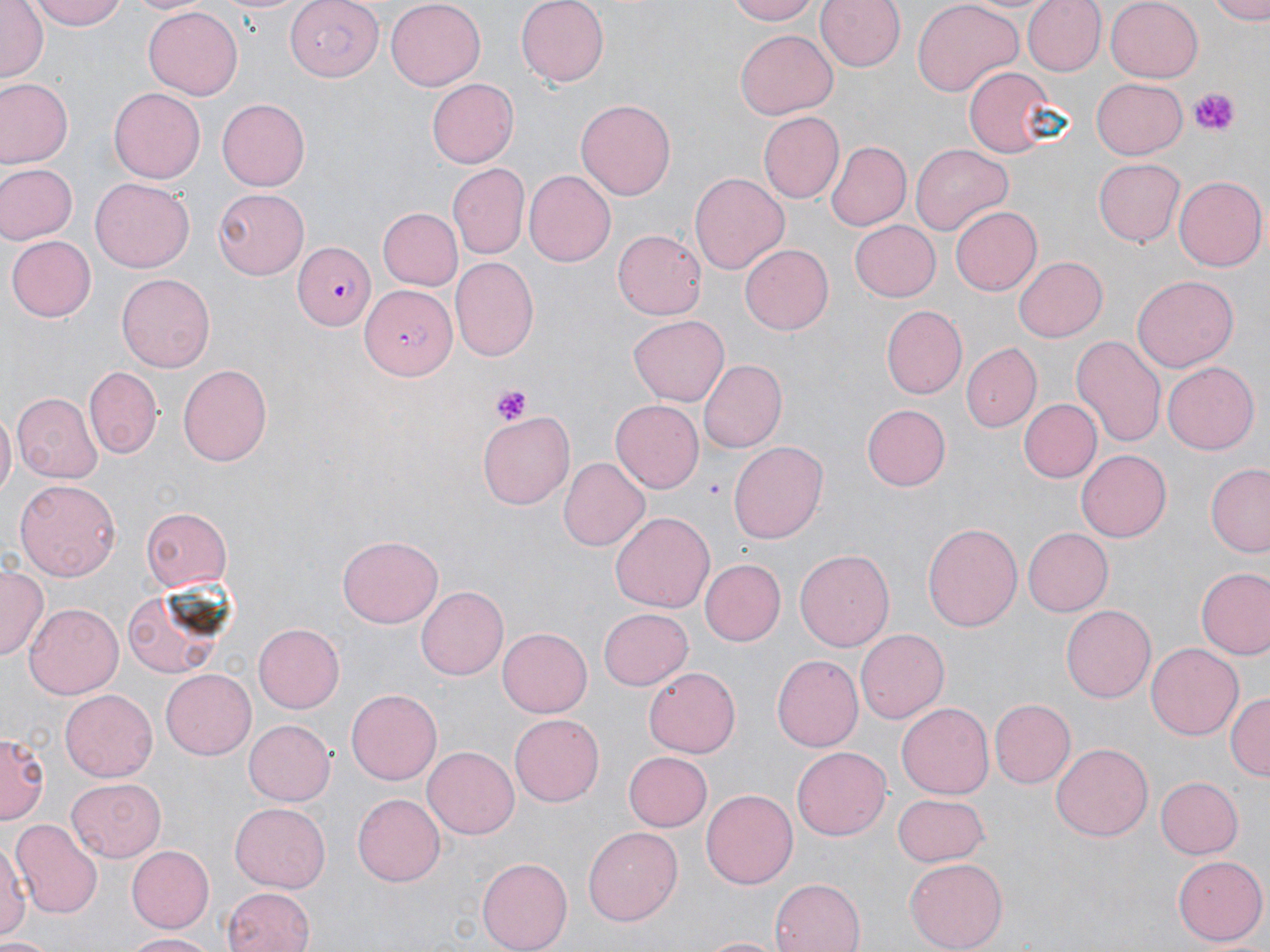
Summary:
  - Coordinate format: approximate bounding boxes as [x1, y1, x2, y2] in pixels
  - Platelet locations: [1191, 87, 1235, 135], [492, 384, 534, 426]
  - Uninfected red blood cell locations: [1, 0, 46, 82], [29, 0, 129, 31], [129, 0, 207, 16], [215, 0, 310, 16], [386, 0, 485, 87], [515, 0, 609, 87], [724, 0, 821, 24], [817, 0, 906, 73], [911, 0, 1026, 97], [1024, 0, 1105, 74], [1104, 0, 1201, 81], [1209, 0, 1270, 23], [143, 6, 244, 101], [734, 29, 836, 119], [964, 66, 1056, 157], [1091, 77, 1187, 161], [426, 78, 518, 169], [1, 79, 72, 165], [109, 87, 207, 183], [216, 96, 309, 189], [575, 98, 676, 201], [758, 110, 843, 201], [825, 142, 909, 232], [911, 143, 1011, 235], [1094, 159, 1184, 246], [0, 162, 77, 244], [448, 163, 529, 259], [523, 171, 616, 268], [690, 172, 788, 271], [1174, 176, 1266, 272], [91, 178, 195, 273], [212, 189, 309, 280], [948, 206, 1040, 297], [375, 207, 463, 290], [849, 219, 941, 301], [614, 228, 707, 320], [7, 234, 97, 322], [741, 245, 833, 335], [1012, 257, 1106, 343], [452, 258, 537, 362], [116, 271, 216, 372], [1133, 276, 1237, 372], [882, 306, 966, 398], [628, 317, 727, 406], [1071, 333, 1167, 452], [963, 344, 1042, 431], [697, 360, 784, 454], [1163, 362, 1258, 455], [177, 364, 273, 466], [84, 367, 161, 457], [11, 393, 101, 483], [1017, 398, 1099, 484], [611, 400, 704, 492], [862, 405, 950, 491], [0, 409, 15, 503], [479, 415, 576, 509], [728, 441, 830, 543], [1077, 449, 1171, 542], [559, 457, 649, 551], [1206, 465, 1270, 555], [14, 478, 121, 580], [140, 508, 233, 592], [609, 511, 715, 614], [922, 519, 1022, 632], [1024, 526, 1113, 616], [336, 536, 441, 628], [794, 548, 895, 651], [699, 559, 784, 646], [0, 566, 47, 657], [1197, 567, 1270, 661], [125, 583, 233, 676], [417, 586, 509, 680], [24, 600, 122, 696], [1060, 605, 1156, 703], [597, 609, 692, 691], [254, 625, 344, 713], [498, 627, 592, 717], [856, 629, 948, 723], [1147, 643, 1243, 741], [773, 655, 862, 751], [645, 667, 740, 758], [162, 670, 255, 758], [61, 687, 159, 780], [346, 687, 442, 785], [1227, 692, 1268, 781], [990, 699, 1075, 787], [897, 702, 994, 800], [509, 714, 605, 806], [244, 719, 336, 806], [1, 728, 47, 827], [1051, 740, 1153, 838], [422, 744, 518, 836], [792, 747, 892, 842], [623, 750, 712, 832], [1153, 776, 1243, 859], [66, 778, 168, 862], [702, 788, 798, 889], [894, 794, 990, 865], [353, 795, 445, 885], [229, 803, 329, 891], [11, 819, 102, 918], [583, 827, 682, 925], [0, 840, 26, 945], [125, 845, 212, 934], [478, 856, 574, 951], [1174, 856, 1266, 944], [903, 857, 1008, 951], [771, 876, 863, 952], [222, 888, 314, 952], [123, 931, 221, 950], [1, 935, 52, 952], [698, 935, 785, 951]
  - Plasmodium falciparum-infected red blood cell locations: [285, 0, 384, 82], [295, 242, 375, 330], [360, 283, 454, 377]
  - Slide-level diagnosis: Plasmodium falciparum
  - Modality: light microscopy
  - Magnification: 1000x
  - Preparation: thin blood smear
  - Stain: May-Grünwald-Giemsa
  - Field of view: one of a larger specimen
  - Image size: 1270×952 pixels